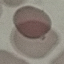

malaria status = uninfected
stain = Giemsa
capture = smartphone through the microscope eyepiece
preparation = thin blood smear
image type = cell patch, automatically extracted from a larger field of view and resized to 64 × 64 pixels